Locate and identify every blood parasite.
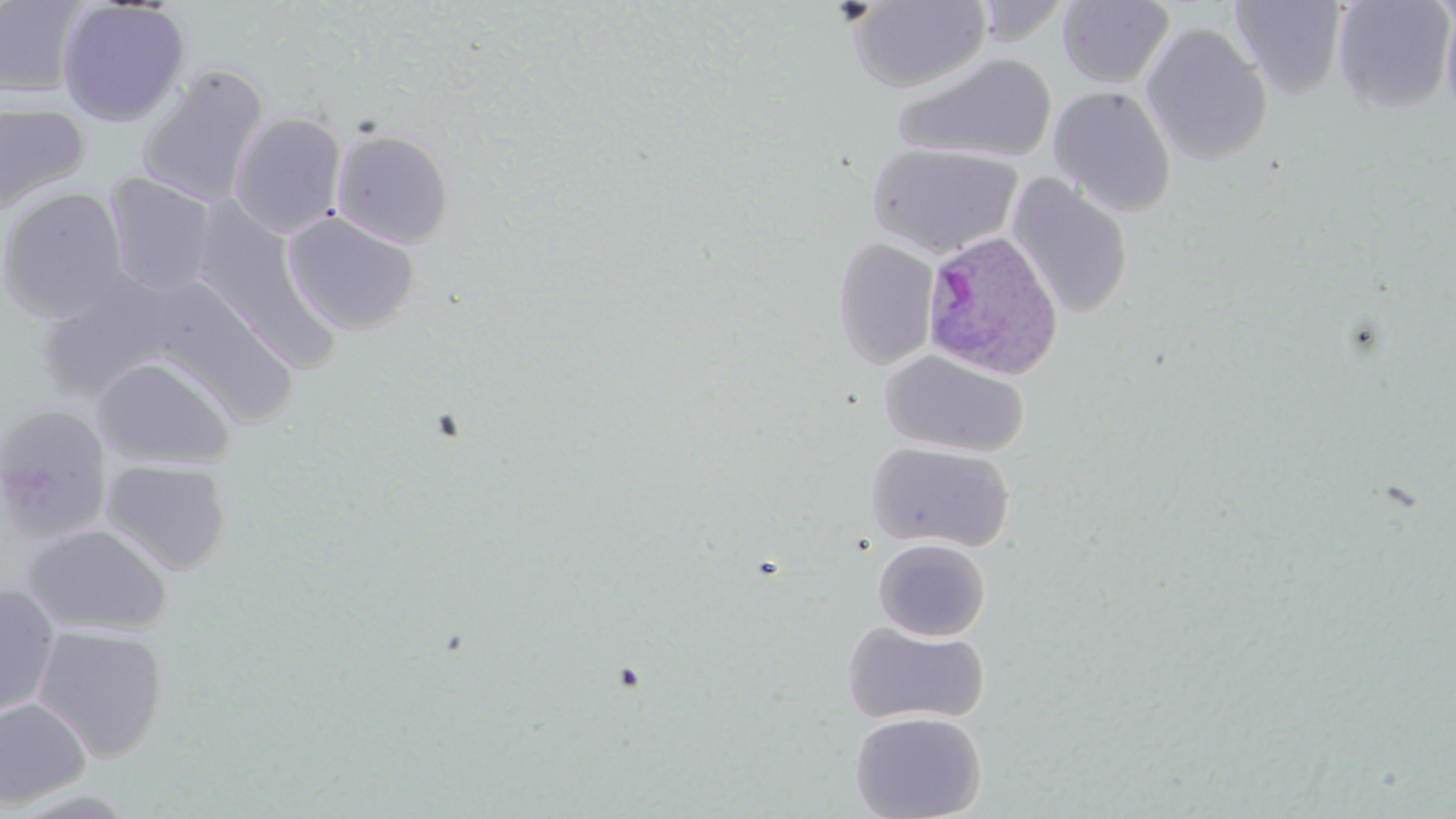
Approximate bounding boxes as (x1, y1, x2, y2) in pixels.
Plasmodium ovale-infected red blood cells: (920, 229, 1064, 381).
No Plasmodium falciparum, Plasmodium malariae, Plasmodium vivax, Babesia divergens, or Trypanosoma brucei observed.

Uninfected red blood cell locations: (972, 0, 1071, 43), (1331, 0, 1456, 114), (1439, 0, 1456, 124), (0, 1, 87, 99), (56, 1, 191, 126), (850, 1, 990, 92), (1058, 1, 1173, 88), (1228, 1, 1348, 99), (1140, 23, 1273, 165), (891, 52, 1057, 164), (136, 64, 270, 209), (1048, 86, 1177, 217), (0, 100, 90, 213), (228, 111, 347, 237), (331, 129, 454, 248), (866, 143, 1023, 258), (104, 172, 217, 298), (1006, 174, 1134, 320), (1, 187, 129, 321), (190, 201, 336, 368), (282, 210, 421, 336), (832, 237, 940, 369), (36, 271, 182, 402), (150, 284, 301, 426), (880, 350, 1028, 457), (92, 355, 237, 469), (0, 404, 113, 539), (865, 441, 1015, 553), (101, 458, 233, 574), (23, 523, 172, 637), (873, 537, 991, 641), (0, 584, 61, 719), (842, 620, 989, 726), (32, 625, 169, 761), (0, 698, 92, 811), (849, 711, 986, 819). Slide-level diagnosis: Plasmodium ovale. Thin blood film. Image is 1456×819 pixels. May-Grünwald-Giemsa-stained preparation. Captured at 1000x magnification. Optical microscopy. Single field of view.